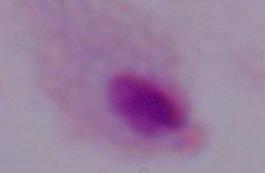
Summary:
  - Identification: trichomonad
  - Modality: photomicrograph
  - Magnification: 1000x